Comment on the morphology of the red blood cells.
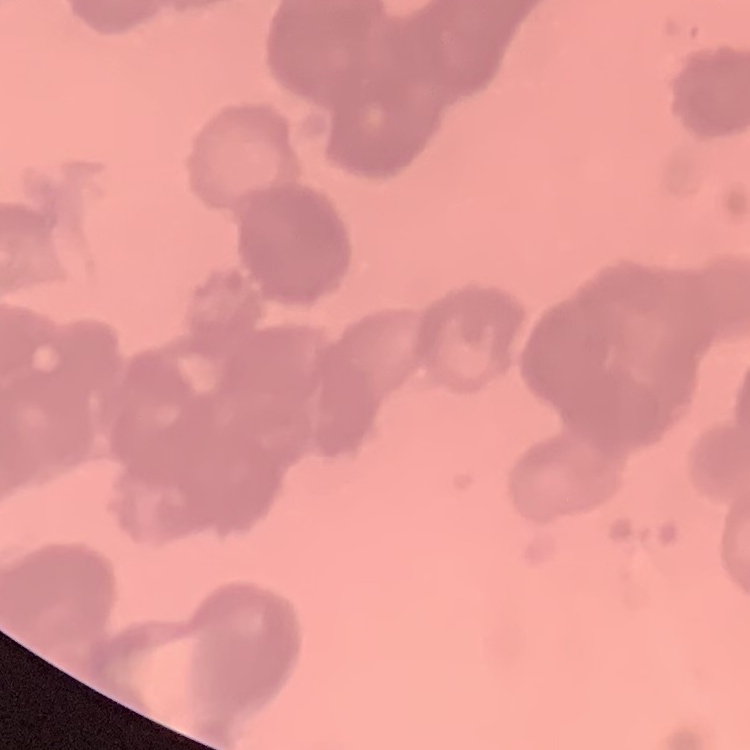

They show rouleaux formation.

Field's or Giemsa stain. Thin peripheral smear. Square crop of a larger photomicrograph.